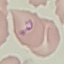

malaria status = uninfected
capture = smartphone camera at the microscope eyepiece
preparation = thin blood smear
stain = Giemsa
image type = cell patch, automatically extracted from a larger field of view and resized to 64 × 64 pixels